State the blood parasite species.
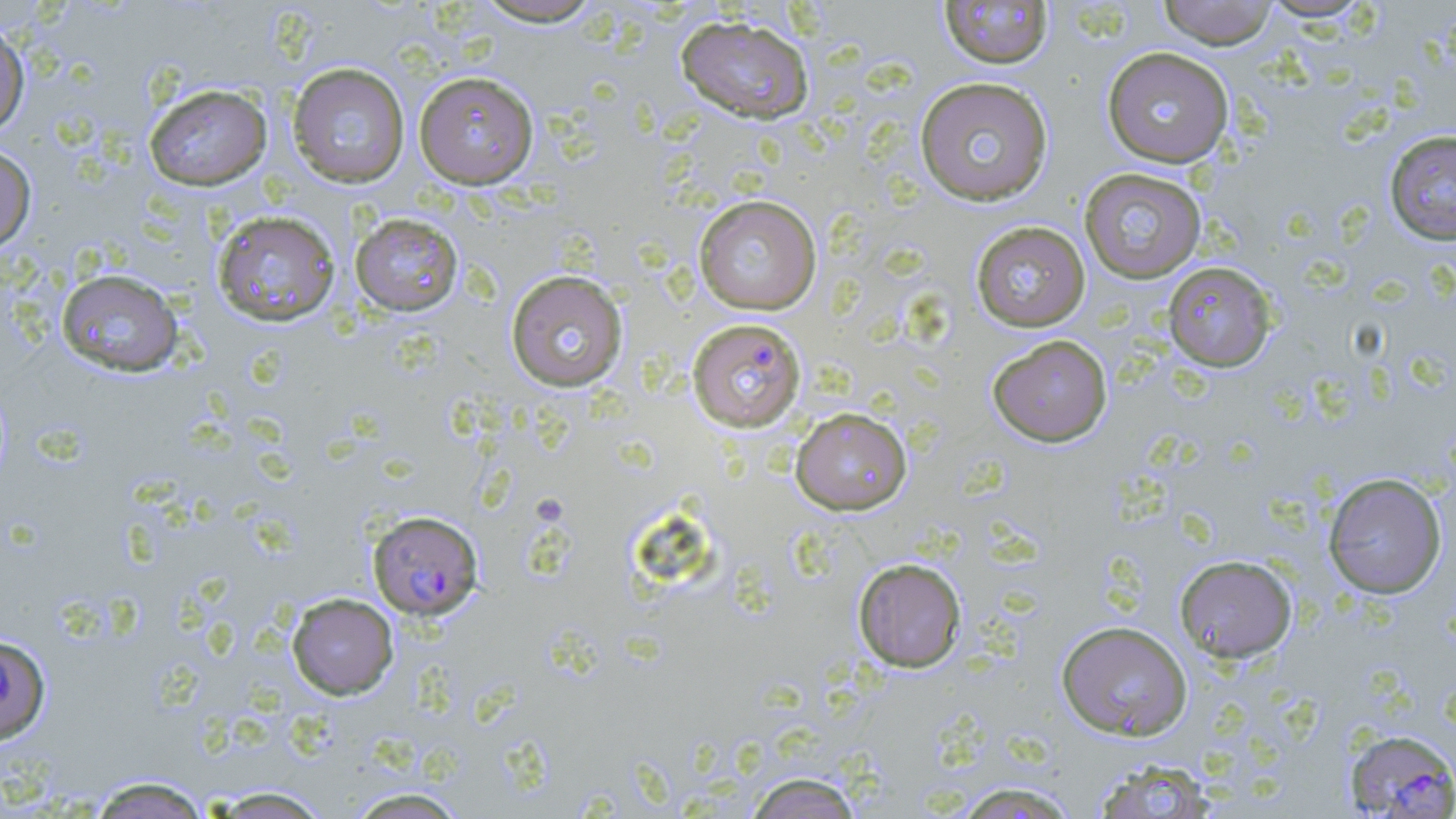

Plasmodium falciparum.

stain: May-Grünwald-Giemsa
image_size: 1456×819 pixels
modality: light microscopy
magnification: 1000x
plasmodium_falciparum_infected_red_blood_cell_locations: 'approximate bounding boxes as named x1/y1/x2/y2 corners in pixels: (x1=686, y1=317, x2=807, y2=432), (x1=368, y1=510, x2=484, y2=620), (x1=0, y1=634, x2=51, y2=744), (x1=1344, y1=728, x2=1456, y2=818)'
preparation: thin blood film
uninfected_red_blood_cell_locations: 'approximate bounding boxes as named x1/y1/x2/y2 corners in pixels: (x1=1157, y1=0, x2=1280, y2=48), (x1=471, y1=1, x2=607, y2=27), (x1=938, y1=1, x2=1054, y2=69), (x1=675, y1=15, x2=814, y2=124), (x1=0, y1=20, x2=30, y2=139), (x1=1101, y1=46, x2=1234, y2=167), (x1=286, y1=62, x2=410, y2=188), (x1=414, y1=71, x2=539, y2=189), (x1=914, y1=76, x2=1054, y2=206), (x1=144, y1=83, x2=273, y2=190), (x1=1384, y1=129, x2=1456, y2=245), (x1=0, y1=143, x2=36, y2=253), (x1=1079, y1=167, x2=1207, y2=284), (x1=693, y1=194, x2=822, y2=315), (x1=211, y1=209, x2=342, y2=327), (x1=350, y1=212, x2=465, y2=316), (x1=970, y1=221, x2=1090, y2=332), (x1=1162, y1=261, x2=1276, y2=372), (x1=55, y1=268, x2=184, y2=377), (x1=505, y1=269, x2=629, y2=392), (x1=987, y1=334, x2=1112, y2=447), (x1=791, y1=407, x2=913, y2=515), (x1=1322, y1=472, x2=1447, y2=599), (x1=1174, y1=554, x2=1298, y2=663), (x1=853, y1=558, x2=967, y2=672), (x1=286, y1=592, x2=399, y2=700), (x1=1056, y1=620, x2=1193, y2=741), (x1=1089, y1=757, x2=1219, y2=819), (x1=743, y1=772, x2=865, y2=819), (x1=87, y1=775, x2=213, y2=819), (x1=950, y1=781, x2=1082, y2=818), (x1=201, y1=786, x2=335, y2=818), (x1=342, y1=787, x2=471, y2=818)'
field_of_view: one of a larger specimen